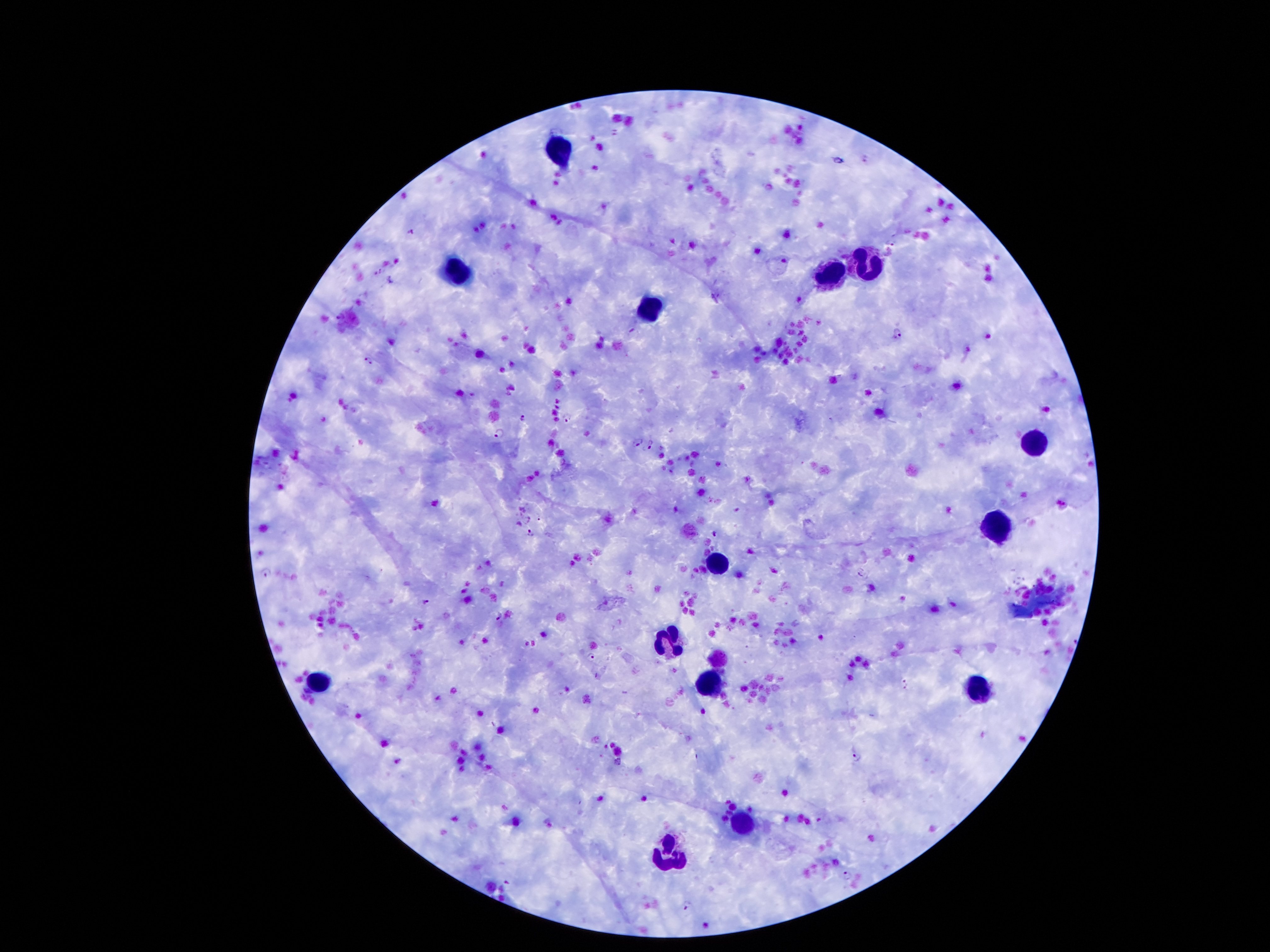 Approximate centers as [x, y] in pixels. Leukocyte locations: [557, 149], [868, 260], [457, 270], [829, 277], [648, 311], [1032, 444], [997, 528], [718, 566], [668, 642], [318, 681], [709, 681], [979, 688], [743, 820], [670, 858]. Plasmodium parasite locations: [839, 159], [897, 333], [367, 360], [567, 416], [523, 417], [499, 432], [636, 441], [651, 446], [530, 532], [715, 534], [266, 572], [862, 572], [426, 601], [499, 617], [822, 637], [592, 655], [905, 680], [906, 688], [855, 757], [846, 875], [507, 883], [687, 904]. Image is 1270×952 pixels. Patient malaria status: positive for Plasmodium falciparum. Photographed through the microscope eyepiece with a smartphone camera. Thick blood film. Single field of view. 100x magnification. Giemsa stain.